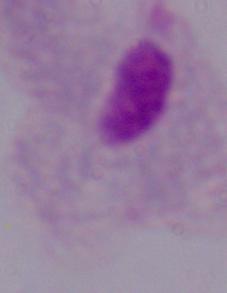

modality = photomicrograph
identification = trichomonad
magnification = 1000x